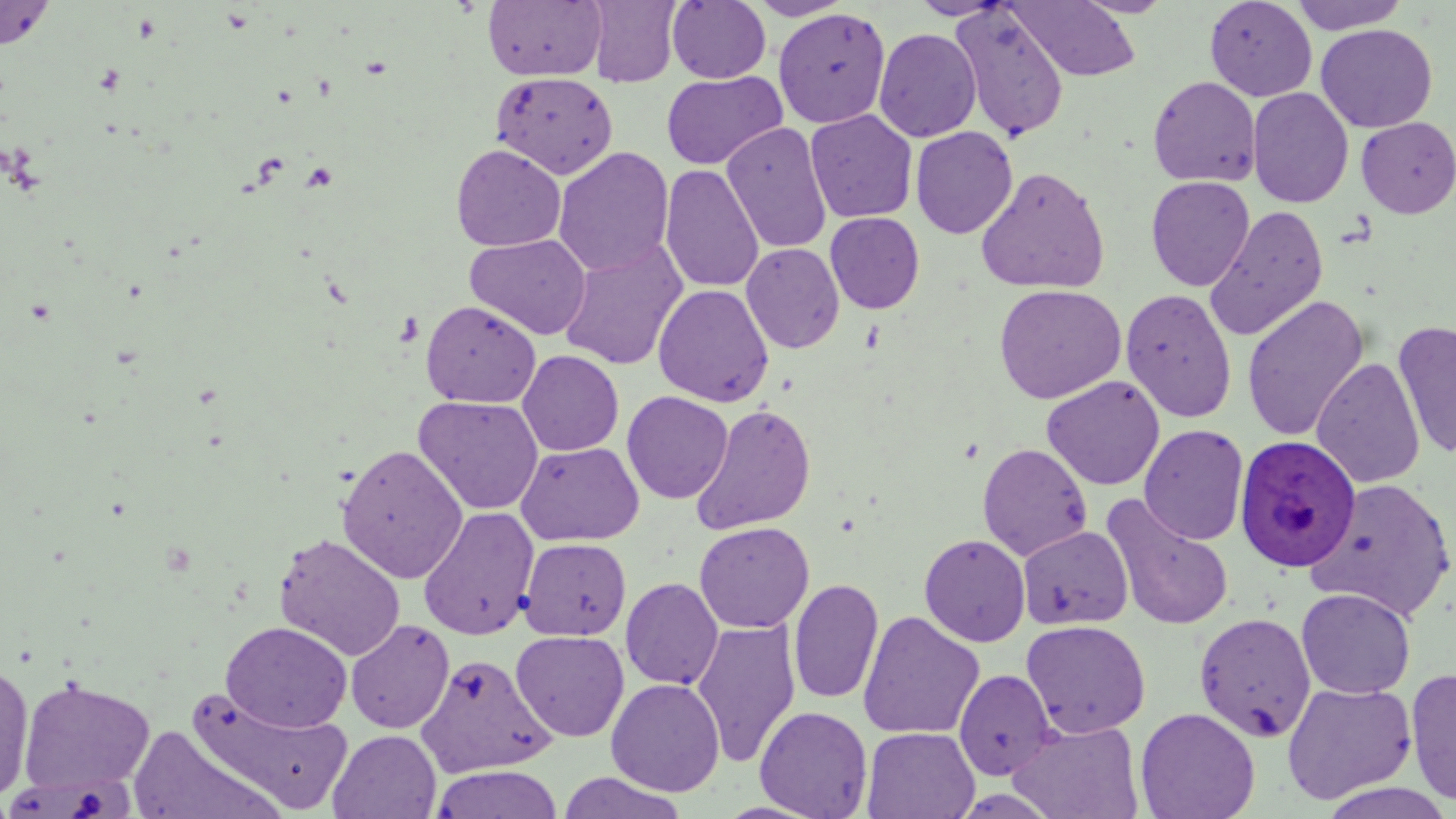
slide-level diagnosis = Plasmodium ovale
magnification = 1000x
preparation = thin blood film
image size = 1456×819 pixels
field of view = one of a larger specimen
uninfected red blood cell locations = approximate bounding boxes as (x1,y1)-(x2,y2) corner pairs in pixels: (0,0)-(56,51), (746,0)-(858,20), (909,0)-(1014,20), (1072,0)-(1176,18), (1204,0)-(1317,101), (1288,0)-(1411,34), (483,1)-(607,82), (585,1)-(682,87), (667,1)-(771,83), (1008,1)-(1141,82), (949,5)-(1070,142), (773,8)-(891,128), (1316,24)-(1438,132), (874,29)-(981,142), (661,71)-(786,169), (491,72)-(619,179), (1148,76)-(1262,188), (1247,87)-(1354,208), (805,110)-(918,223), (1356,117)-(1456,218), (721,123)-(832,253), (910,126)-(1018,239), (451,144)-(566,251), (553,147)-(675,277), (660,164)-(764,293), (975,166)-(1110,294), (1145,176)-(1254,291), (1204,205)-(1329,341), (825,212)-(925,314), (466,234)-(591,340), (558,240)-(687,370), (741,242)-(844,354), (993,283)-(1126,404), (653,284)-(774,407), (1120,288)-(1237,424), (1242,295)-(1369,442), (421,300)-(541,408), (1392,320)-(1456,460), (518,350)-(624,456), (1312,357)-(1425,490), (1042,375)-(1165,490), (622,391)-(733,504), (413,395)-(544,515), (689,403)-(817,535), (1139,424)-(1249,545), (515,441)-(644,546), (977,442)-(1093,561), (336,443)-(468,583), (1307,478)-(1456,621), (1099,494)-(1236,632), (418,506)-(540,640), (694,521)-(814,634), (1017,524)-(1133,631), (273,532)-(406,661), (919,533)-(1031,647), (519,537)-(631,640), (621,577)-(724,690), (788,578)-(884,705), (1296,588)-(1416,699), (858,611)-(984,740), (1194,611)-(1316,743), (345,618)-(455,733), (691,620)-(801,767), (1020,620)-(1151,738), (220,621)-(353,733), (510,630)-(629,742), (415,653)-(555,777), (0,657)-(35,804), (1404,665)-(1456,808), (954,668)-(1057,779), (18,677)-(155,795), (606,678)-(725,796), (1281,681)-(1417,804), (186,688)-(353,816), (755,706)-(873,818), (1135,707)-(1260,819), (1009,720)-(1143,818), (126,725)-(282,819), (862,727)-(979,818), (328,729)-(442,819), (430,765)-(564,819), (558,771)-(688,819)
Plasmodium ovale-infected red blood cell locations = approximate bounding boxes as (x1,y1)-(x2,y2) corner pairs in pixels: (1234,435)-(1361,572)
stain = May-Grünwald-Giemsa
modality = optical microscopy